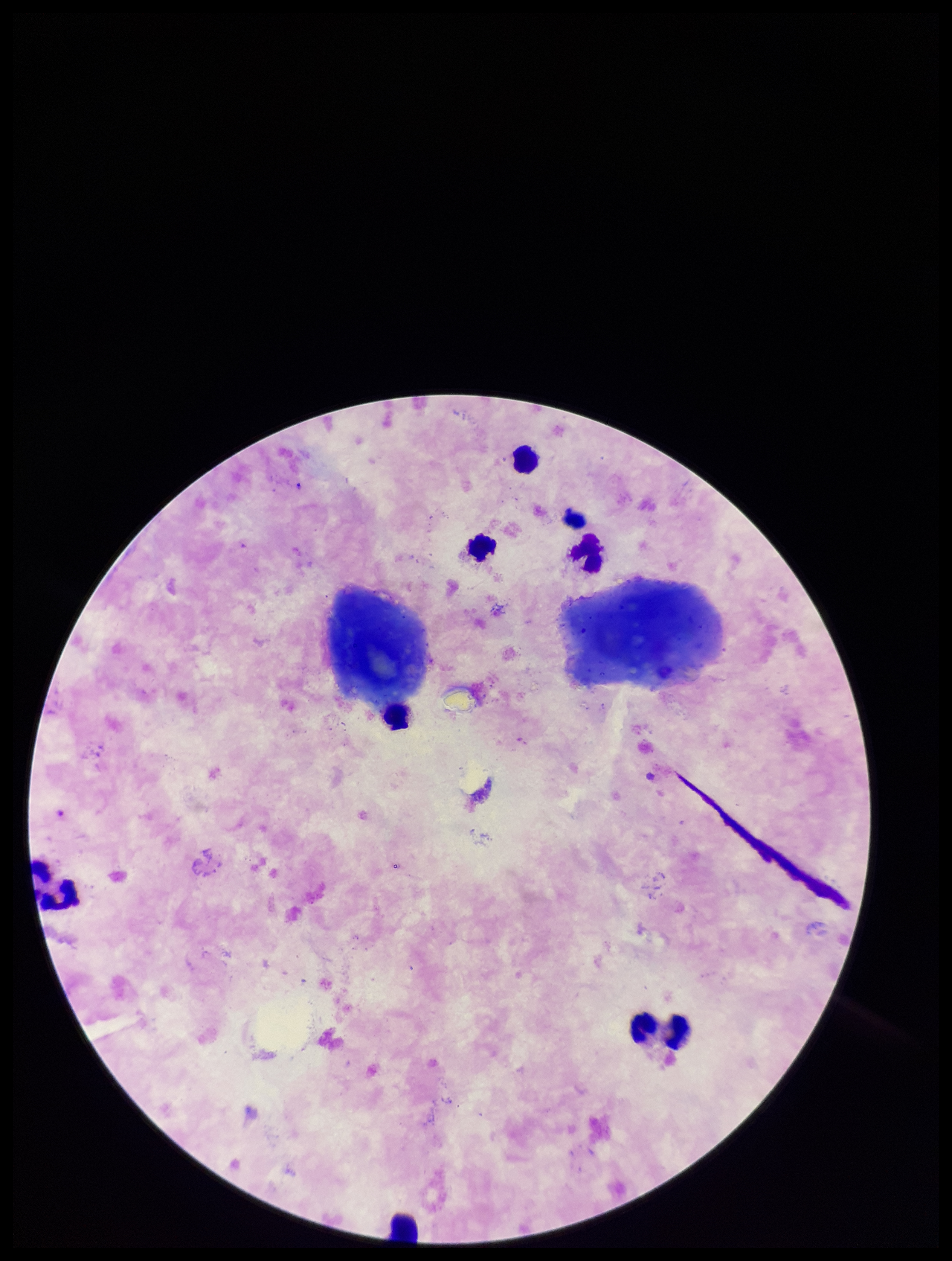
Summary:
  - Plasmodium parasites: none identified
  - Field of view: single
  - Image size: 952×1261 pixels
  - Patient malaria status: positive
  - Leukocyte count: 8
  - Parasite count: 0
  - Preparation: thick smear
  - Stain: Giemsa
  - Capture: smartphone photograph through the microscope eyepiece
  - Species reported for this patient: Plasmodium falciparum